Identify the blood parasite species.
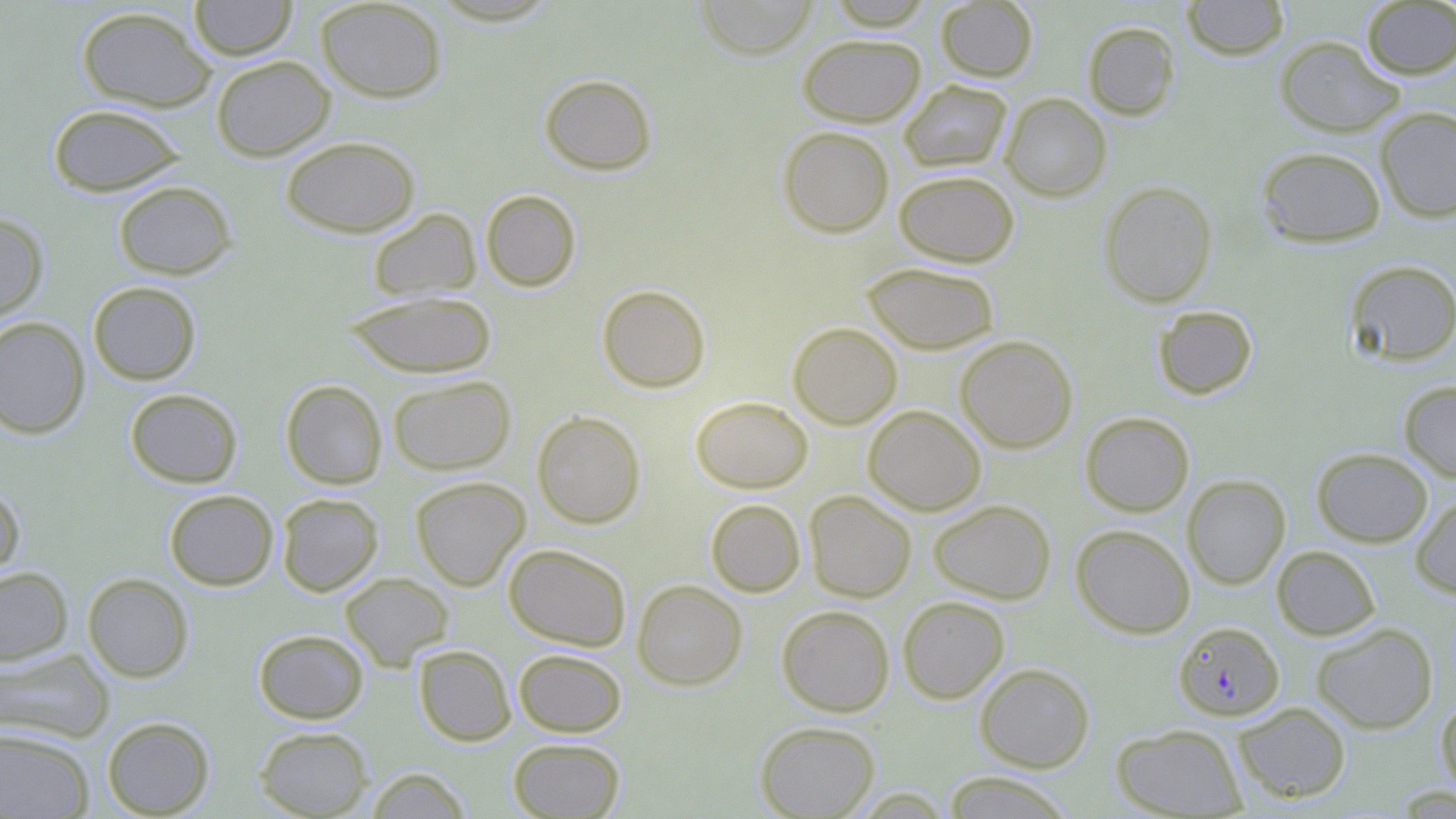
Plasmodium falciparum.

uninfected red blood cell locations = approximate bounding boxes as [x1, y1, x2, y2] in pixels: [189, 0, 297, 61], [314, 0, 448, 103], [822, 0, 937, 30], [1180, 0, 1290, 61], [695, 1, 819, 58], [935, 1, 1039, 82], [1361, 1, 1456, 79], [76, 5, 216, 112], [1082, 21, 1181, 120], [797, 33, 926, 126], [1274, 35, 1405, 137], [211, 56, 335, 161], [539, 73, 658, 175], [899, 80, 1013, 173], [999, 93, 1112, 201], [47, 103, 186, 197], [1374, 106, 1456, 222], [778, 126, 894, 237], [280, 135, 420, 237], [1255, 145, 1387, 248], [894, 170, 1019, 267], [113, 180, 236, 279], [1098, 180, 1218, 308], [480, 189, 581, 291], [368, 208, 481, 301], [0, 213, 48, 321], [1345, 260, 1456, 366], [862, 261, 1000, 354], [88, 281, 202, 385], [597, 284, 711, 393], [343, 290, 497, 378], [1152, 305, 1258, 400], [0, 316, 90, 439], [788, 322, 903, 429], [955, 335, 1078, 453], [388, 374, 515, 475], [280, 380, 387, 489], [1398, 380, 1456, 483], [125, 388, 243, 488], [690, 396, 813, 493], [863, 405, 986, 515], [531, 410, 646, 529], [1080, 411, 1194, 517], [1311, 447, 1433, 547], [1182, 474, 1290, 589], [410, 476, 530, 590], [0, 481, 25, 585], [164, 489, 279, 590], [803, 490, 917, 602], [276, 493, 384, 596], [1410, 494, 1456, 598], [706, 499, 805, 597], [928, 499, 1056, 604], [1070, 524, 1196, 638], [503, 543, 631, 651], [1272, 545, 1381, 640], [0, 566, 73, 666], [82, 572, 194, 682], [340, 572, 454, 670], [632, 579, 747, 690], [897, 596, 1009, 703], [776, 604, 894, 716], [1311, 622, 1438, 733], [253, 629, 369, 723], [414, 645, 515, 746], [0, 648, 114, 744], [513, 648, 627, 737], [975, 662, 1095, 772], [1435, 694, 1456, 799], [1233, 701, 1351, 803], [101, 716, 214, 817], [755, 721, 880, 818], [1112, 723, 1247, 817], [254, 725, 373, 818], [0, 727, 94, 818], [508, 737, 626, 818], [365, 767, 471, 818], [942, 771, 1075, 818]
stain = May-Grünwald-Giemsa
field of view = single
image size = 1456×819 pixels
Plasmodium falciparum-infected red blood cell locations = approximate bounding boxes as [x1, y1, x2, y2] in pixels: [1173, 621, 1284, 721]
modality = optical microscopy
magnification = 1000x
preparation = thin blood smear